Assess for malaria.
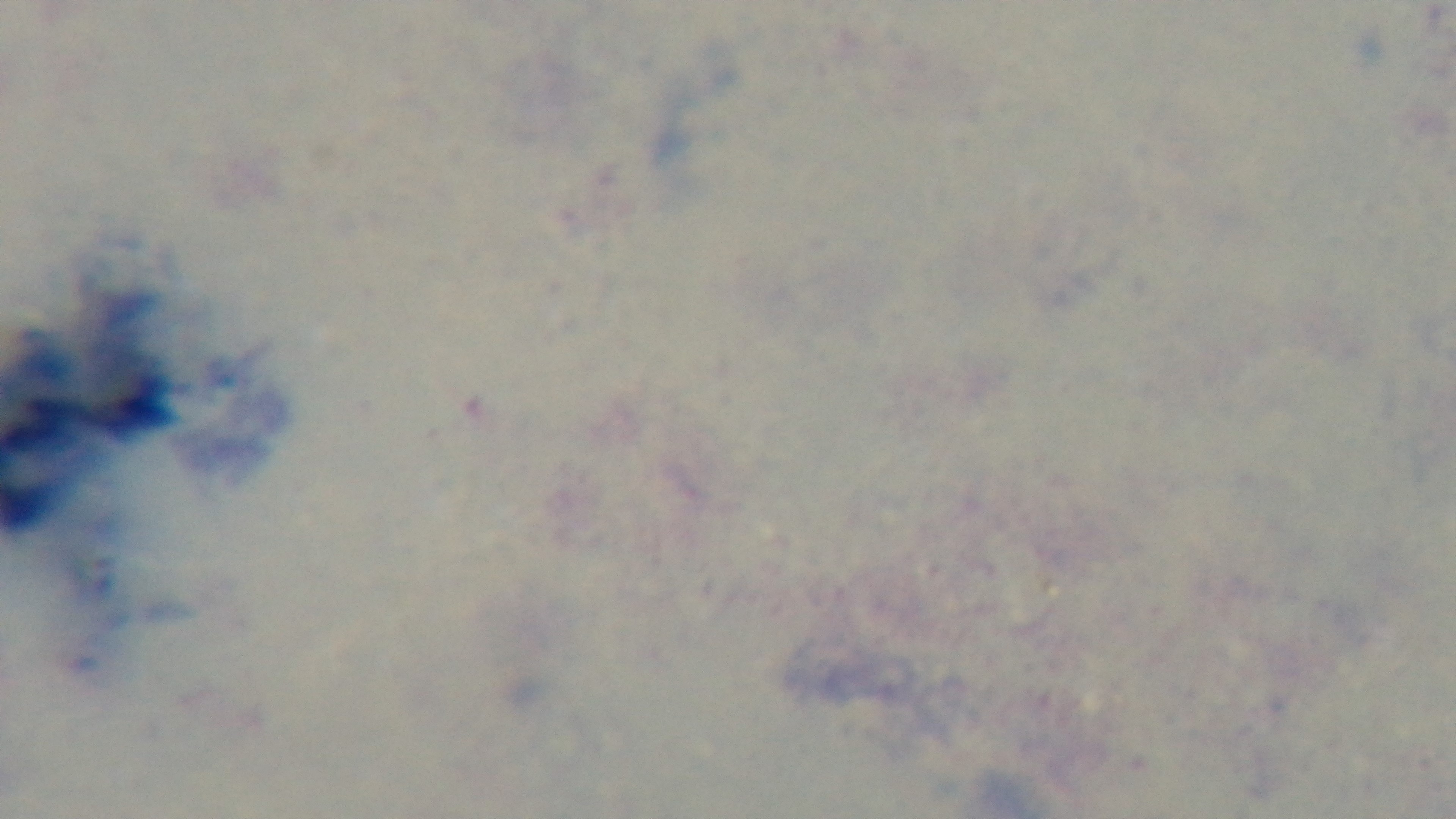

Uninfected.

Summary:
  - Field of view: one from the slide
  - Modality: light microscopy
  - Objective: 100x oil immersion
  - Stain: Giemsa
  - Capture: mounted 4K digital camera
  - Preparation: thick